Comment on the morphology of the erythrocytes.
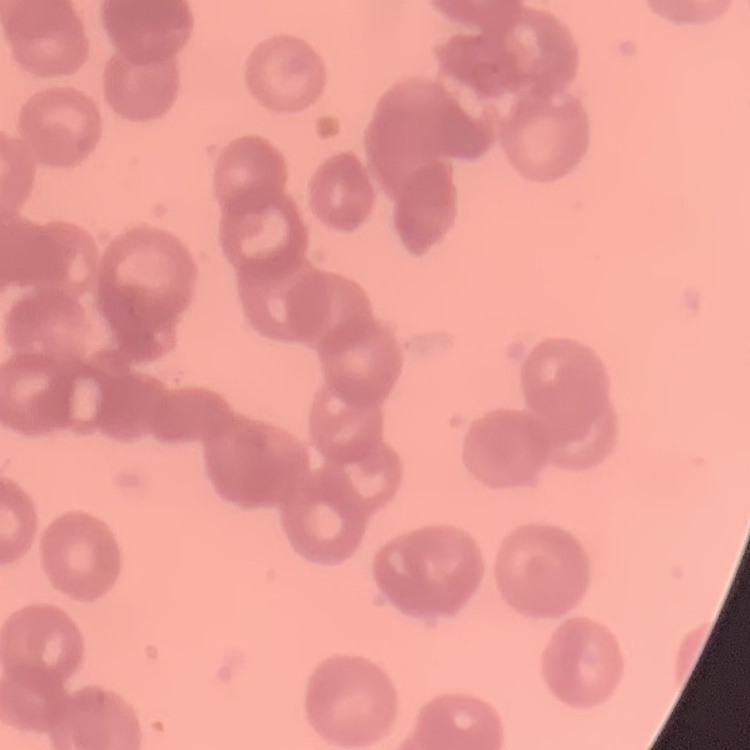

Rouleaux formation.

preparation: thin peripheral smear
image_type: square crop of a larger photomicrograph
stain: Field's or Giemsa